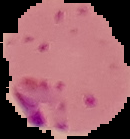
{
  "malaria_status": "parasitized",
  "image_type": "segmented cell region with the area outside set to black",
  "preparation": "thin blood smear",
  "image_size": "130×139 pixels"
}